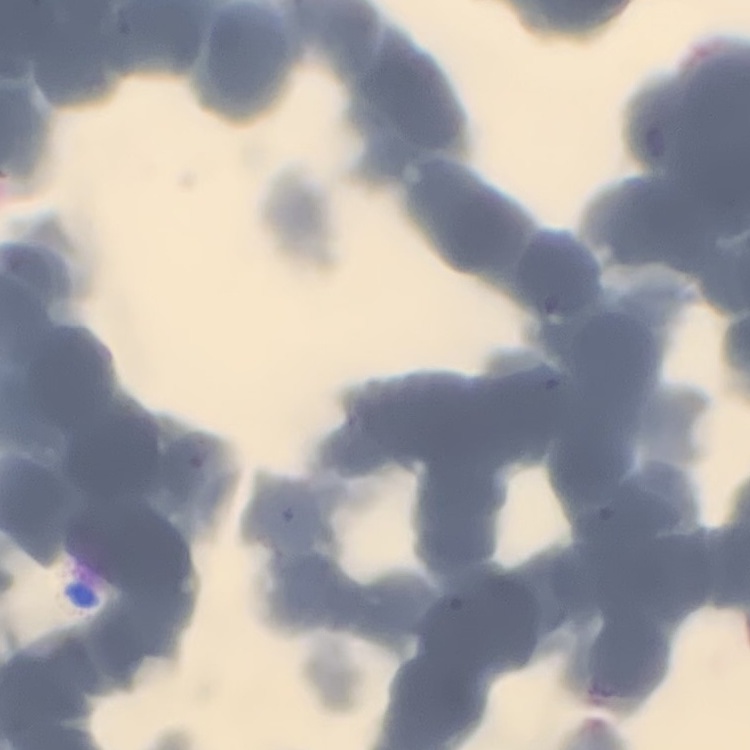
{
  "erythrocyte_morphology": "rouleaux formation",
  "image_type": "square crop of a larger photomicrograph",
  "stain": "Field's or Giemsa",
  "preparation": "thin blood film"
}